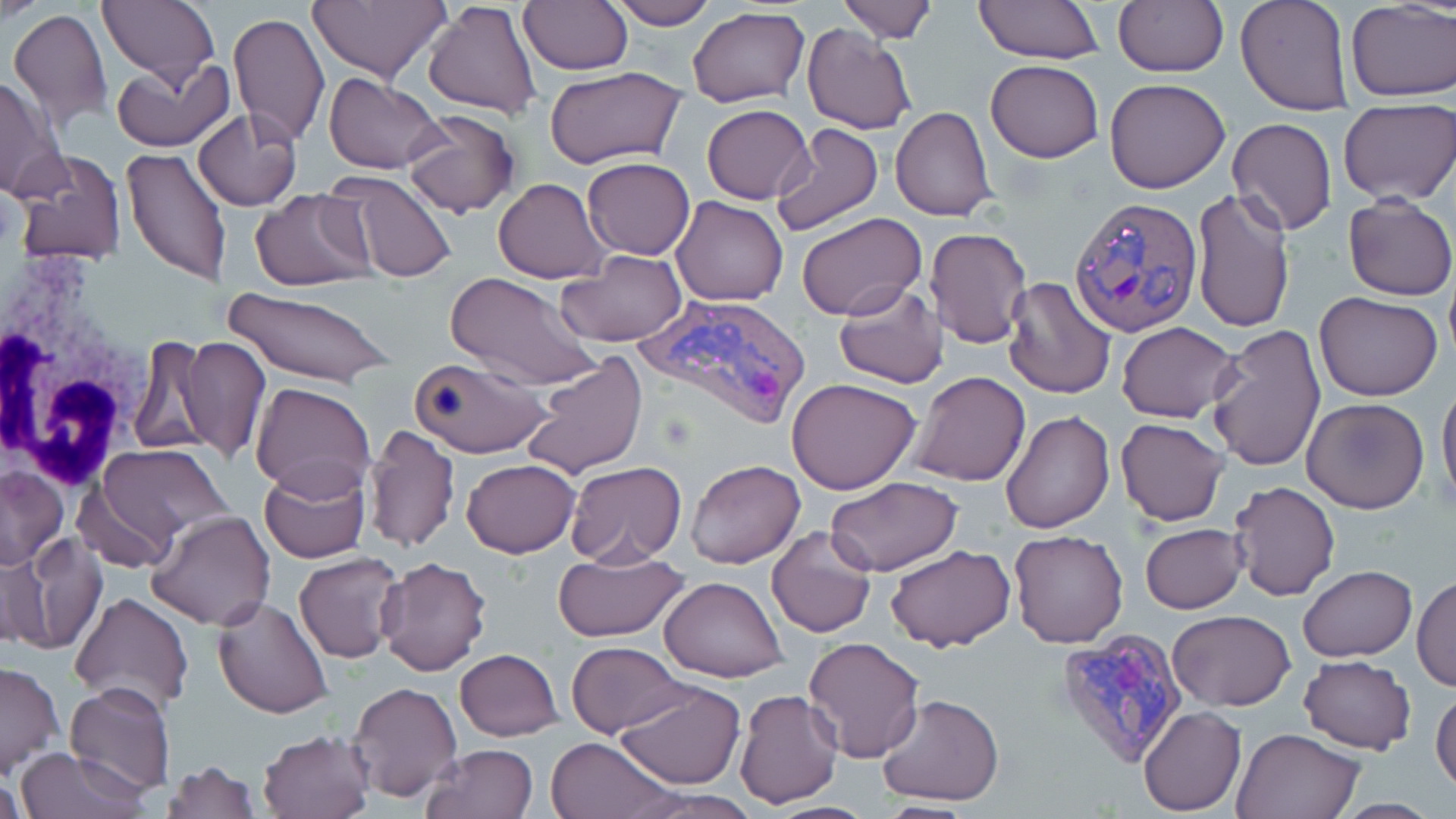

Approximate bounding boxes as named x1/y1/x2/y2 corners in pixels. Uninfected red blood cell locations: (x1=0, y1=0, x2=44, y2=19), (x1=306, y1=0, x2=451, y2=84), (x1=422, y1=0, x2=543, y2=119), (x1=605, y1=0, x2=719, y2=30), (x1=837, y1=0, x2=938, y2=43), (x1=974, y1=0, x2=1103, y2=63), (x1=1235, y1=0, x2=1353, y2=115), (x1=518, y1=1, x2=634, y2=75), (x1=97, y1=2, x2=219, y2=88), (x1=1113, y1=2, x2=1228, y2=76), (x1=1345, y1=2, x2=1455, y2=100), (x1=687, y1=7, x2=811, y2=108), (x1=8, y1=8, x2=113, y2=133), (x1=228, y1=13, x2=327, y2=146), (x1=801, y1=25, x2=917, y2=135), (x1=109, y1=56, x2=232, y2=152), (x1=985, y1=60, x2=1103, y2=163), (x1=546, y1=67, x2=685, y2=169), (x1=322, y1=72, x2=446, y2=174), (x1=1, y1=75, x2=68, y2=199), (x1=1104, y1=78, x2=1230, y2=193), (x1=1338, y1=103, x2=1456, y2=204), (x1=701, y1=104, x2=814, y2=204), (x1=890, y1=105, x2=997, y2=221), (x1=193, y1=107, x2=302, y2=211), (x1=400, y1=108, x2=520, y2=218), (x1=1226, y1=118, x2=1337, y2=235), (x1=769, y1=122, x2=884, y2=238), (x1=121, y1=146, x2=231, y2=286), (x1=12, y1=149, x2=126, y2=264), (x1=582, y1=157, x2=695, y2=260), (x1=324, y1=172, x2=460, y2=284), (x1=493, y1=178, x2=611, y2=284), (x1=244, y1=185, x2=379, y2=385), (x1=1192, y1=187, x2=1295, y2=336), (x1=250, y1=189, x2=374, y2=287), (x1=1343, y1=195, x2=1456, y2=301), (x1=672, y1=196, x2=787, y2=306), (x1=796, y1=212, x2=926, y2=322), (x1=924, y1=227, x2=1030, y2=348), (x1=558, y1=251, x2=686, y2=348), (x1=445, y1=271, x2=602, y2=391), (x1=1003, y1=275, x2=1118, y2=401), (x1=832, y1=283, x2=950, y2=389), (x1=225, y1=288, x2=395, y2=386), (x1=1314, y1=291, x2=1444, y2=401), (x1=1116, y1=321, x2=1241, y2=423), (x1=1206, y1=324, x2=1327, y2=475), (x1=127, y1=333, x2=216, y2=458), (x1=178, y1=336, x2=270, y2=461), (x1=522, y1=352, x2=647, y2=481), (x1=409, y1=354, x2=555, y2=457), (x1=907, y1=370, x2=1031, y2=487), (x1=1437, y1=373, x2=1456, y2=513), (x1=786, y1=378, x2=921, y2=495), (x1=250, y1=381, x2=376, y2=497), (x1=1302, y1=397, x2=1430, y2=513), (x1=1001, y1=409, x2=1115, y2=534), (x1=1115, y1=417, x2=1228, y2=527), (x1=363, y1=424, x2=461, y2=556), (x1=89, y1=444, x2=232, y2=562), (x1=462, y1=458, x2=580, y2=558), (x1=686, y1=459, x2=805, y2=569), (x1=258, y1=461, x2=372, y2=564), (x1=564, y1=461, x2=687, y2=567), (x1=0, y1=466, x2=68, y2=569), (x1=825, y1=475, x2=964, y2=576), (x1=1227, y1=481, x2=1340, y2=601), (x1=146, y1=509, x2=276, y2=629), (x1=1140, y1=523, x2=1247, y2=613), (x1=767, y1=525, x2=878, y2=639), (x1=1007, y1=529, x2=1128, y2=647), (x1=6, y1=532, x2=105, y2=656), (x1=884, y1=543, x2=1016, y2=652), (x1=552, y1=549, x2=690, y2=642), (x1=292, y1=552, x2=406, y2=664), (x1=374, y1=556, x2=491, y2=678), (x1=1298, y1=566, x2=1417, y2=662), (x1=1413, y1=574, x2=1455, y2=693), (x1=659, y1=575, x2=788, y2=681), (x1=70, y1=592, x2=195, y2=712), (x1=211, y1=595, x2=335, y2=718), (x1=1167, y1=611, x2=1296, y2=709), (x1=803, y1=637, x2=926, y2=762), (x1=566, y1=641, x2=689, y2=737), (x1=455, y1=649, x2=563, y2=741), (x1=1297, y1=655, x2=1417, y2=754), (x1=0, y1=663, x2=64, y2=777), (x1=348, y1=681, x2=463, y2=803), (x1=64, y1=682, x2=176, y2=798), (x1=615, y1=682, x2=746, y2=790), (x1=1433, y1=683, x2=1456, y2=800), (x1=734, y1=689, x2=843, y2=809), (x1=876, y1=694, x2=1006, y2=805), (x1=1139, y1=706, x2=1247, y2=816), (x1=1231, y1=728, x2=1363, y2=818), (x1=257, y1=729, x2=374, y2=818), (x1=544, y1=735, x2=677, y2=819), (x1=421, y1=744, x2=541, y2=819), (x1=13, y1=746, x2=149, y2=819), (x1=159, y1=759, x2=261, y2=818), (x1=0, y1=770, x2=25, y2=819), (x1=1334, y1=798, x2=1438, y2=817). Plasmodium vivax-infected red blood cell locations: (x1=1068, y1=196, x2=1204, y2=337), (x1=633, y1=295, x2=808, y2=433), (x1=1054, y1=630, x2=1189, y2=767). White blood cell locations: (x1=0, y1=263, x2=160, y2=493). Slide-level diagnosis: Plasmodium vivax. Single field of view. Thin blood smear. Optical microscopy. May-Grünwald-Giemsa stain. 1000x magnification. Image is 1456×819 pixels.